Locate every Plasmodium parasite.
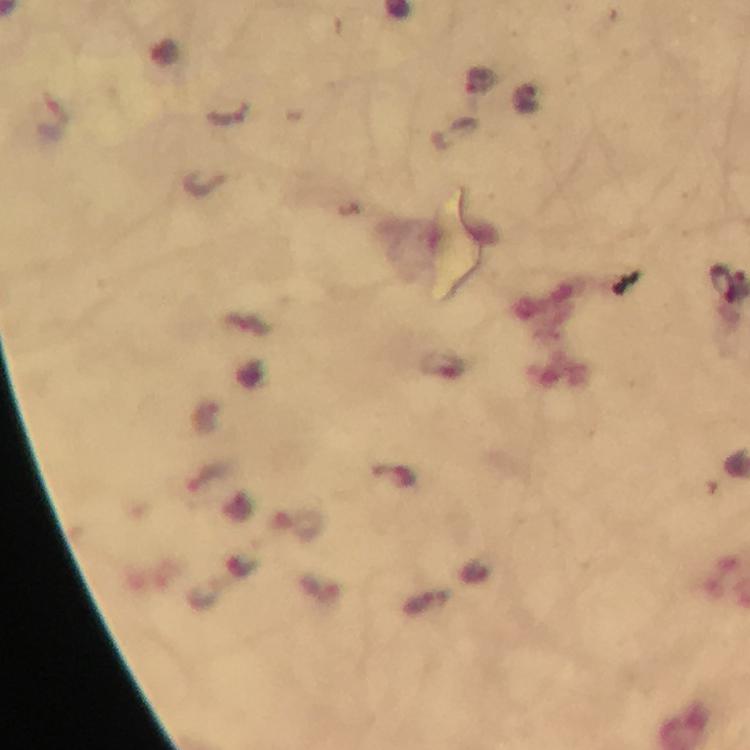

Approximate object centers, in pixels from the top-left corner.
Plasmodium parasites: (x=479, y=80), (x=722, y=283).

{
  "capture": "smartphone mounted on the microscope",
  "context": "from a diagnostic examination for malaria",
  "magnification": "100x",
  "image_size": "750×750 pixels",
  "cropped_from": "a single field of view",
  "immersion_oil": "used",
  "preparation": "thick blood film",
  "stain": "Giemsa"
}